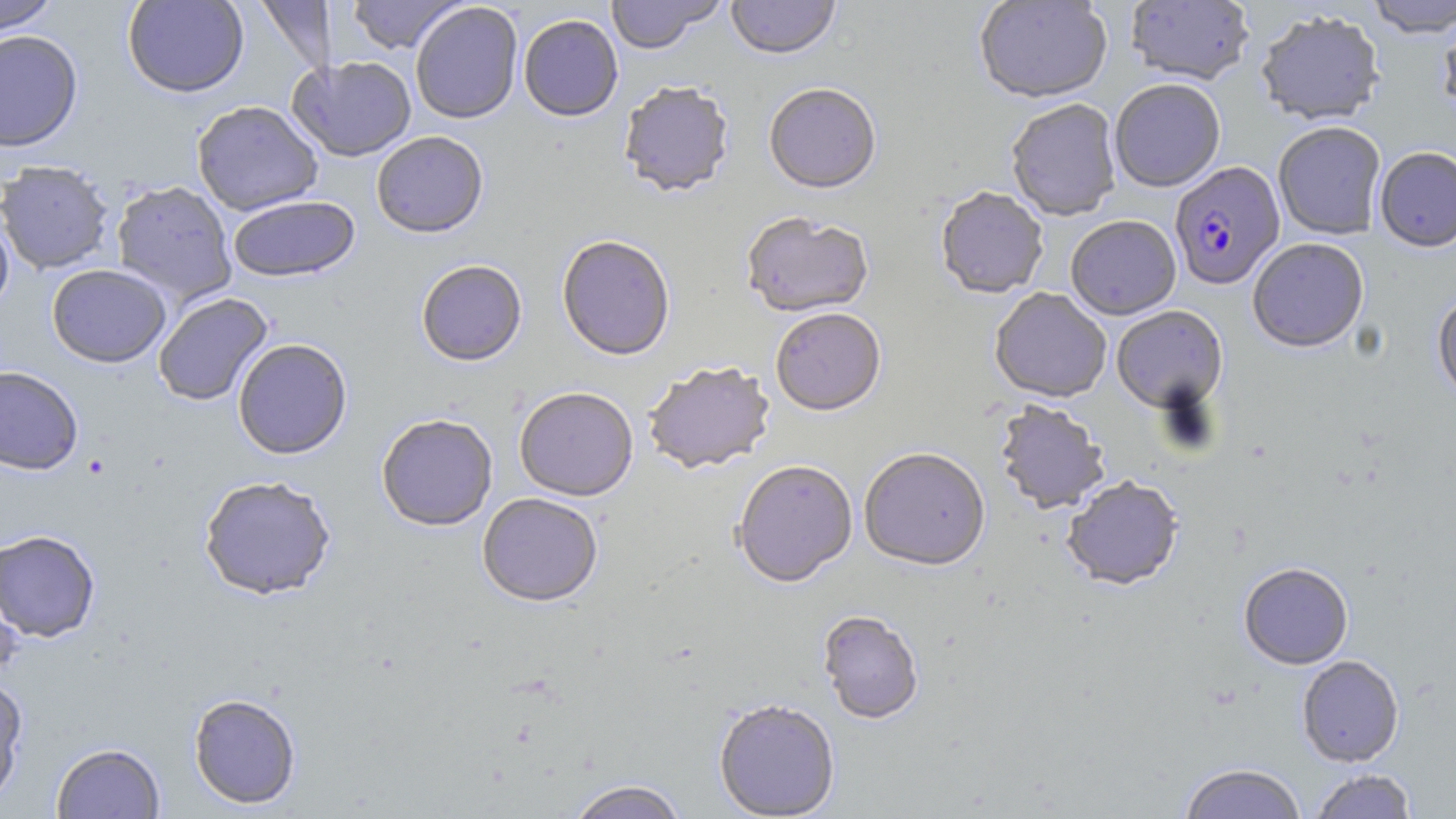 Approximate bounding boxes as (x1,y1)-(x2,y2) corner pairs in pixels. Plasmodium falciparum-infected red blood cell locations: (1170,163)-(1284,291). Uninfected red blood cell locations: (0,0)-(60,36), (122,0)-(249,98), (347,0)-(468,55), (606,0)-(725,55), (726,0)-(841,62), (974,0)-(1112,106), (1125,0)-(1254,86), (1364,0)-(1456,38), (257,1)-(335,78), (410,3)-(523,125), (1255,10)-(1386,126), (1437,10)-(1456,122), (519,16)-(623,123), (0,29)-(83,152), (288,56)-(417,163), (1110,81)-(1226,193), (619,84)-(735,201), (764,86)-(881,197), (191,100)-(324,216), (1006,101)-(1121,223), (1273,122)-(1387,240), (372,133)-(489,240), (1374,146)-(1456,252), (0,160)-(115,274), (111,180)-(237,306), (935,189)-(1048,301), (228,196)-(360,283), (0,207)-(15,318), (740,214)-(874,321), (1066,218)-(1181,321), (556,238)-(675,362), (1247,239)-(1368,354), (416,262)-(527,369), (47,263)-(171,367), (989,289)-(1111,404), (1432,290)-(1456,403), (154,293)-(273,406), (1112,307)-(1227,414), (771,311)-(886,419), (233,339)-(352,460), (643,364)-(776,477), (0,365)-(84,475), (514,389)-(638,504), (993,402)-(1110,516), (376,416)-(497,533), (859,450)-(990,575), (732,463)-(858,590), (198,475)-(337,600), (1062,478)-(1183,593), (477,494)-(603,609), (0,529)-(101,642), (1239,564)-(1353,670), (0,568)-(25,681), (817,612)-(923,726), (1297,656)-(1404,767), (0,676)-(28,805), (188,693)-(301,810), (714,702)-(840,818), (51,742)-(165,818), (1178,764)-(1307,819), (1309,769)-(1417,818), (566,781)-(688,819). Slide-level diagnosis: Plasmodium falciparum. 1000x magnification. May-Grünwald-Giemsa stain. Thin blood film. Image is 1456×819 pixels. Light microscopy. Single field of view.